Assess this cell for malaria.
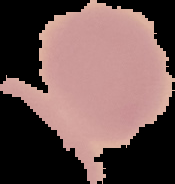
It is uninfected.

preparation = thin blood smear
image type = segmented cell region with the area outside set to black
image size = 175×184 pixels